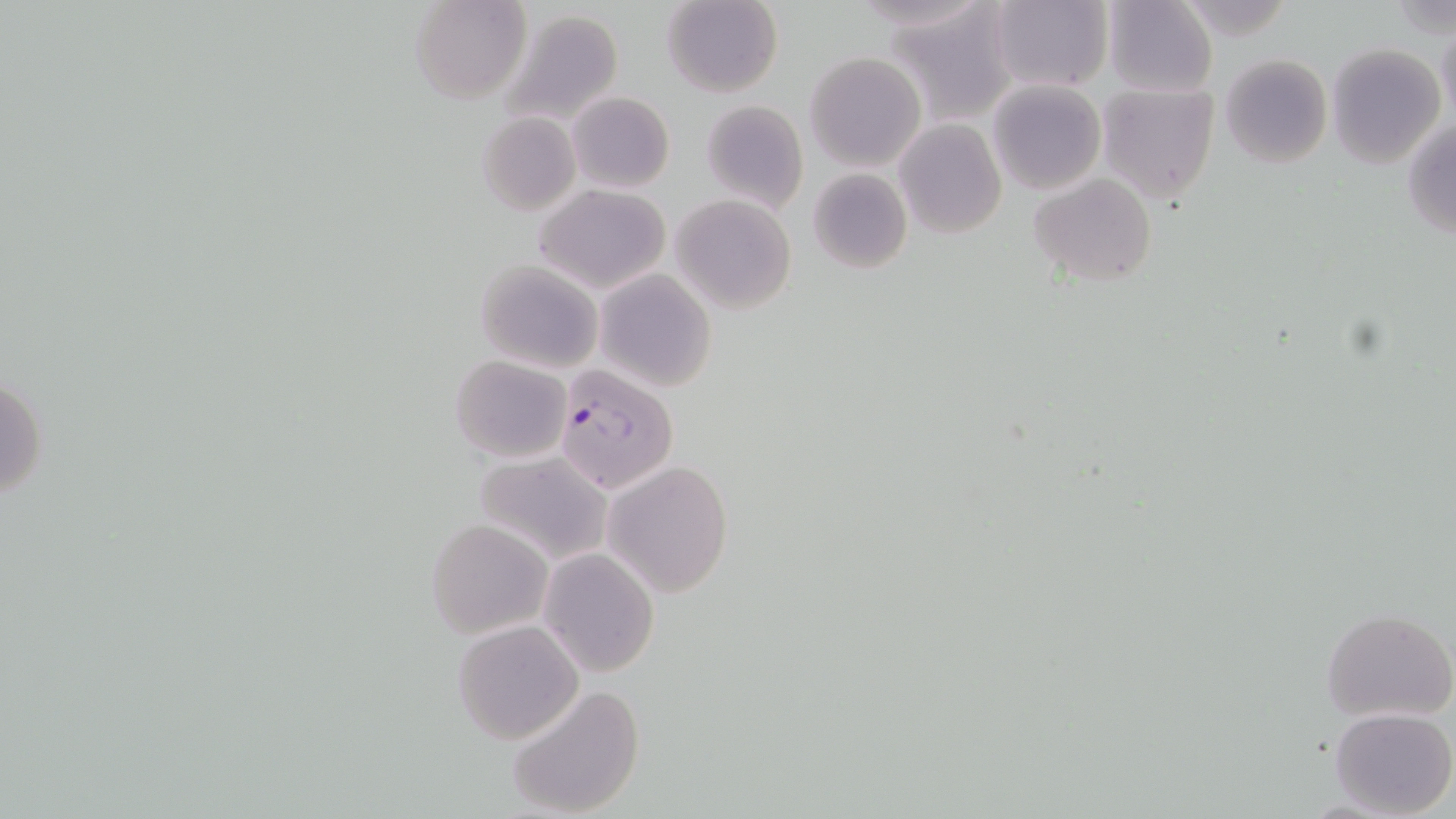
Summary:
  - Coordinate format: approximate bounding boxes as named x1/y1/x2/y2 corners in pixels
  - Plasmodium falciparum-infected red blood cell locations: (x1=554, y1=356, x2=674, y2=497)
  - Uninfected red blood cell locations: (x1=410, y1=0, x2=531, y2=105), (x1=661, y1=0, x2=783, y2=98), (x1=989, y1=1, x2=1112, y2=92), (x1=1102, y1=1, x2=1218, y2=95), (x1=885, y1=3, x2=1015, y2=123), (x1=497, y1=11, x2=624, y2=129), (x1=1437, y1=21, x2=1456, y2=122), (x1=1325, y1=43, x2=1447, y2=168), (x1=804, y1=52, x2=926, y2=171), (x1=1220, y1=54, x2=1333, y2=170), (x1=987, y1=80, x2=1104, y2=194), (x1=1095, y1=81, x2=1219, y2=203), (x1=567, y1=91, x2=675, y2=193), (x1=700, y1=100, x2=808, y2=215), (x1=478, y1=111, x2=582, y2=217), (x1=894, y1=119, x2=1006, y2=239), (x1=1403, y1=119, x2=1456, y2=240), (x1=807, y1=168, x2=912, y2=274), (x1=1029, y1=173, x2=1158, y2=287), (x1=535, y1=183, x2=671, y2=295), (x1=671, y1=194, x2=798, y2=314), (x1=474, y1=260, x2=602, y2=374), (x1=595, y1=268, x2=718, y2=391), (x1=450, y1=355, x2=572, y2=462), (x1=1, y1=369, x2=46, y2=506), (x1=474, y1=450, x2=614, y2=569), (x1=606, y1=459, x2=733, y2=597), (x1=425, y1=517, x2=552, y2=638), (x1=539, y1=547, x2=660, y2=677), (x1=1322, y1=607, x2=1455, y2=723), (x1=451, y1=619, x2=584, y2=743), (x1=506, y1=683, x2=646, y2=818), (x1=1328, y1=707, x2=1456, y2=818)
  - Slide-level diagnosis: Plasmodium falciparum
  - Image size: 1456×819 pixels
  - Field of view: one of a larger specimen
  - Magnification: 1000x
  - Stain: May-Grünwald-Giemsa
  - Preparation: thin blood smear
  - Modality: optical microscopy